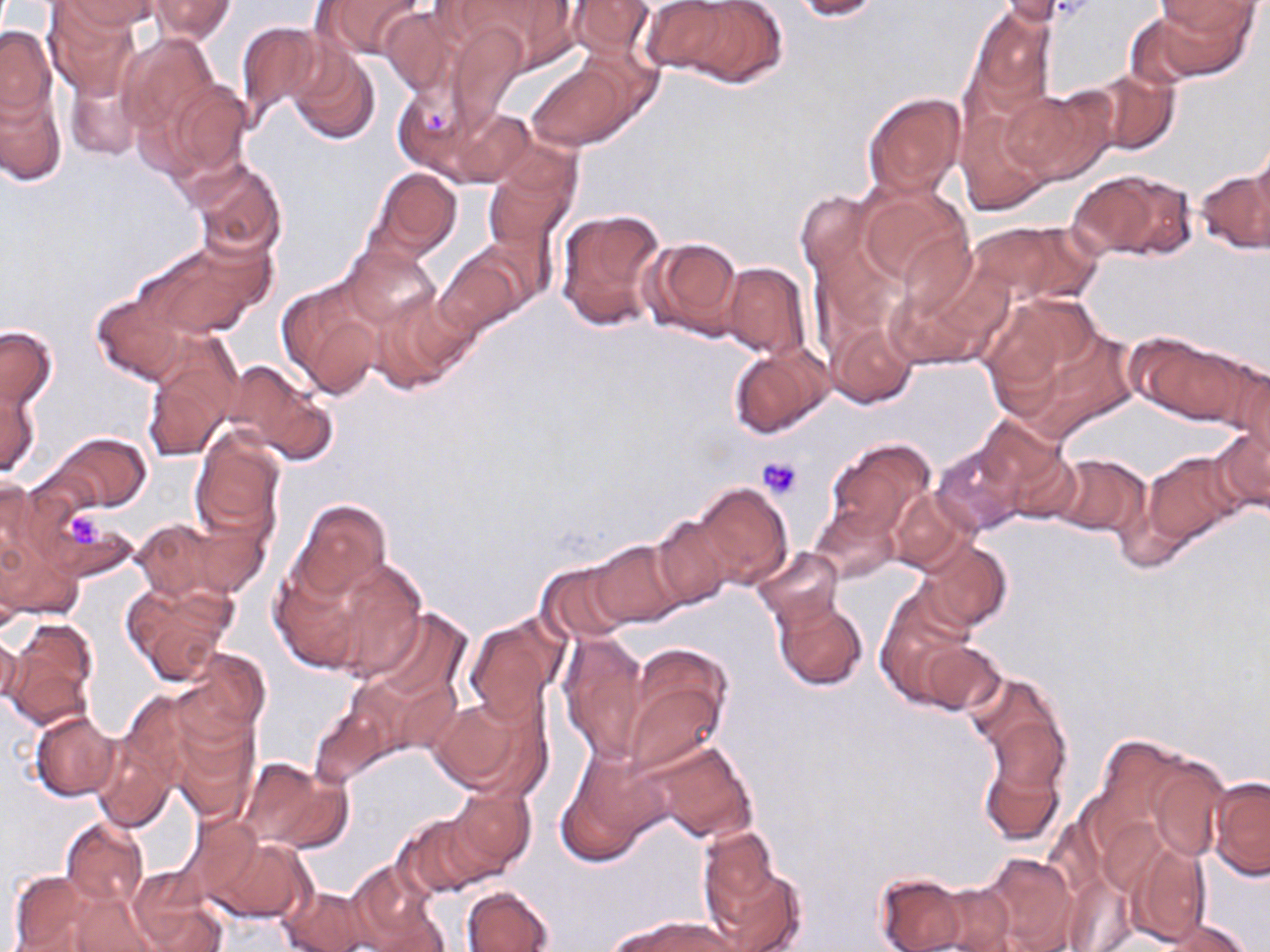
Summary:
  - Coordinate format: approximate bounding boxes as named x1/y1/x2/y2 corners in pixels
  - Platelet locations: (x1=421, y1=107, x2=450, y2=132), (x1=758, y1=457, x2=803, y2=500), (x1=54, y1=508, x2=114, y2=558)
  - Uninfected red blood cell locations: (x1=44, y1=0, x2=140, y2=99), (x1=55, y1=0, x2=159, y2=35), (x1=148, y1=0, x2=235, y2=43), (x1=322, y1=0, x2=427, y2=58), (x1=459, y1=0, x2=582, y2=65), (x1=566, y1=0, x2=655, y2=60), (x1=635, y1=0, x2=742, y2=74), (x1=790, y1=0, x2=882, y2=20), (x1=998, y1=0, x2=1088, y2=28), (x1=674, y1=1, x2=788, y2=89), (x1=1159, y1=1, x2=1260, y2=35), (x1=1143, y1=4, x2=1256, y2=80), (x1=967, y1=5, x2=1056, y2=114), (x1=381, y1=6, x2=461, y2=96), (x1=447, y1=21, x2=526, y2=125), (x1=236, y1=22, x2=328, y2=124), (x1=0, y1=25, x2=56, y2=120), (x1=117, y1=33, x2=219, y2=137), (x1=288, y1=45, x2=380, y2=144), (x1=528, y1=63, x2=632, y2=150), (x1=65, y1=65, x2=144, y2=163), (x1=1088, y1=67, x2=1180, y2=154), (x1=160, y1=80, x2=253, y2=182), (x1=393, y1=82, x2=483, y2=177), (x1=0, y1=84, x2=66, y2=187), (x1=1002, y1=88, x2=1108, y2=183), (x1=864, y1=93, x2=965, y2=199), (x1=450, y1=106, x2=535, y2=186), (x1=956, y1=108, x2=1053, y2=215), (x1=1248, y1=134, x2=1270, y2=229), (x1=190, y1=159, x2=286, y2=261), (x1=482, y1=159, x2=576, y2=249), (x1=370, y1=167, x2=461, y2=259), (x1=1067, y1=168, x2=1197, y2=261), (x1=1193, y1=168, x2=1269, y2=255), (x1=856, y1=187, x2=972, y2=296), (x1=796, y1=192, x2=873, y2=274), (x1=557, y1=208, x2=667, y2=334), (x1=971, y1=220, x2=1098, y2=307), (x1=136, y1=236, x2=269, y2=339), (x1=641, y1=236, x2=744, y2=339), (x1=338, y1=244, x2=440, y2=333), (x1=435, y1=248, x2=528, y2=335), (x1=722, y1=263, x2=810, y2=359), (x1=883, y1=272, x2=999, y2=369), (x1=278, y1=280, x2=387, y2=400), (x1=369, y1=289, x2=475, y2=394), (x1=91, y1=291, x2=191, y2=385), (x1=983, y1=292, x2=1113, y2=423), (x1=827, y1=319, x2=917, y2=409), (x1=0, y1=324, x2=58, y2=416), (x1=1128, y1=333, x2=1260, y2=426), (x1=142, y1=339, x2=240, y2=461), (x1=730, y1=344, x2=831, y2=438), (x1=1228, y1=359, x2=1270, y2=471), (x1=223, y1=361, x2=334, y2=462), (x1=1, y1=378, x2=41, y2=478), (x1=969, y1=417, x2=1067, y2=505), (x1=1209, y1=421, x2=1270, y2=514), (x1=191, y1=430, x2=285, y2=541), (x1=50, y1=433, x2=152, y2=512), (x1=825, y1=439, x2=934, y2=539), (x1=933, y1=442, x2=1027, y2=535), (x1=1135, y1=449, x2=1249, y2=556), (x1=1004, y1=451, x2=1084, y2=524), (x1=1051, y1=453, x2=1149, y2=535), (x1=0, y1=474, x2=39, y2=571), (x1=690, y1=482, x2=792, y2=588), (x1=889, y1=488, x2=979, y2=575), (x1=291, y1=499, x2=391, y2=599), (x1=809, y1=503, x2=900, y2=584), (x1=42, y1=507, x2=135, y2=579), (x1=131, y1=516, x2=245, y2=603), (x1=651, y1=517, x2=735, y2=610), (x1=0, y1=527, x2=82, y2=624), (x1=916, y1=538, x2=1010, y2=632), (x1=588, y1=539, x2=687, y2=629), (x1=753, y1=547, x2=844, y2=630), (x1=270, y1=552, x2=410, y2=677), (x1=537, y1=561, x2=635, y2=644), (x1=336, y1=576, x2=453, y2=694), (x1=121, y1=582, x2=235, y2=685), (x1=877, y1=595, x2=979, y2=706), (x1=773, y1=596, x2=869, y2=691), (x1=366, y1=608, x2=471, y2=706), (x1=464, y1=613, x2=567, y2=721), (x1=5, y1=620, x2=100, y2=728), (x1=0, y1=632, x2=22, y2=707), (x1=559, y1=633, x2=649, y2=762), (x1=921, y1=639, x2=1005, y2=716), (x1=181, y1=647, x2=271, y2=738), (x1=623, y1=661, x2=728, y2=774), (x1=967, y1=671, x2=1066, y2=772), (x1=431, y1=693, x2=545, y2=799), (x1=310, y1=705, x2=391, y2=786), (x1=165, y1=707, x2=258, y2=822), (x1=30, y1=712, x2=121, y2=801), (x1=92, y1=736, x2=177, y2=833), (x1=1102, y1=740, x2=1229, y2=871), (x1=647, y1=742, x2=756, y2=843), (x1=979, y1=756, x2=1064, y2=846), (x1=239, y1=757, x2=341, y2=850), (x1=556, y1=765, x2=658, y2=864), (x1=1209, y1=776, x2=1269, y2=880), (x1=443, y1=788, x2=536, y2=878), (x1=396, y1=813, x2=496, y2=899), (x1=182, y1=815, x2=265, y2=905), (x1=61, y1=818, x2=148, y2=909), (x1=698, y1=826, x2=783, y2=916), (x1=209, y1=837, x2=311, y2=923), (x1=1122, y1=845, x2=1213, y2=946), (x1=978, y1=852, x2=1080, y2=952), (x1=706, y1=856, x2=805, y2=952), (x1=347, y1=862, x2=444, y2=950), (x1=7, y1=869, x2=100, y2=951), (x1=129, y1=872, x2=224, y2=951), (x1=872, y1=873, x2=968, y2=952), (x1=930, y1=882, x2=1016, y2=952), (x1=461, y1=885, x2=556, y2=952), (x1=279, y1=887, x2=371, y2=952), (x1=64, y1=893, x2=163, y2=951), (x1=611, y1=915, x2=736, y2=952), (x1=1147, y1=916, x2=1254, y2=952)
  - Slide-level diagnosis: no evidence of blood parasites
  - Modality: light microscopy
  - Stain: May-Grünwald-Giemsa
  - Magnification: 1000x
  - Field of view: single
  - Image size: 1270×952 pixels
  - Preparation: thin blood smear